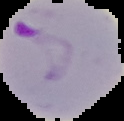
From a thin blood smear. The area outside the segmented cell region is set to black. Malaria status: parasitized. Image is 124×121 pixels.